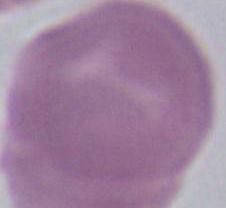

Summary:
  - Identification: red blood cell
  - Modality: micrograph
  - Magnification: 1000x